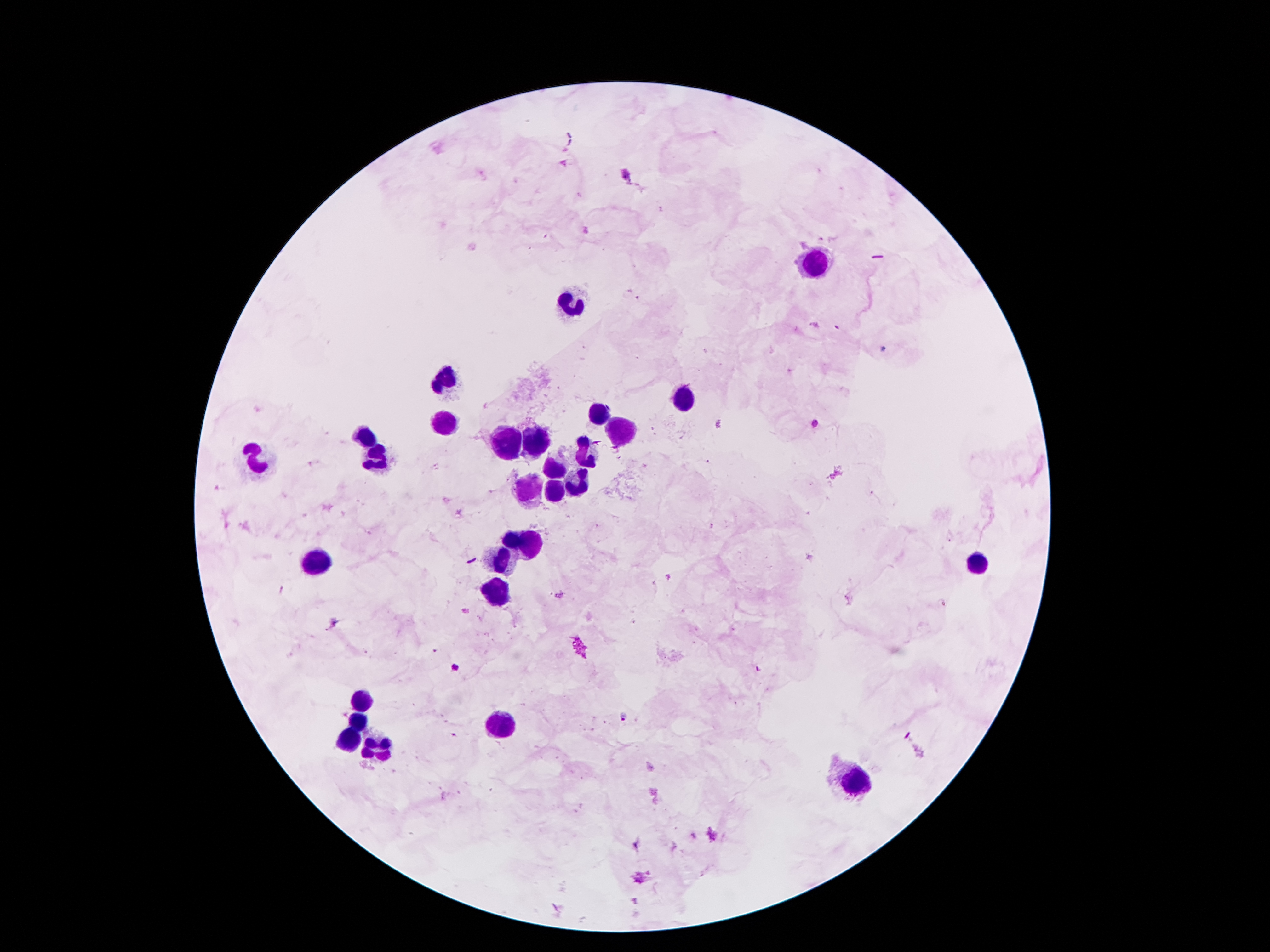

coordinate format = approximate centers as [x, y] in pixels
Plasmodium parasite locations = [626, 173], [718, 424], [456, 668], [626, 718]
leukocyte locations = [813, 265], [566, 302], [443, 377], [684, 399], [600, 411], [445, 426], [622, 433], [365, 438], [508, 442], [538, 442], [583, 449], [377, 458], [250, 463], [554, 470], [579, 485], [531, 488], [556, 490], [525, 538], [500, 558], [318, 563], [977, 565], [499, 592], [361, 701], [357, 720], [499, 726], [350, 738], [373, 747], [856, 785]
preparation = thick blood film
capture = smartphone through the microscope eyepiece
magnification = 100x
image size = 1270×952 pixels
stain = Giemsa
field of view = one from this slide
patient malaria status = infected with Plasmodium falciparum